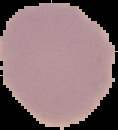
Summary:
  - Preparation: thin blood smear
  - Image size: 118×130 pixels
  - Result: negative for malaria parasites
  - Image type: segmented cell region with the area outside set to black